Assess this cell for malaria.
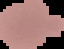

Uninfected.

From a thin blood smear. Image is 64×49 pixels. The area outside the segmented cell region is set to black.